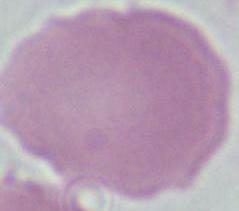
identification: erythrocyte
modality: micrograph
magnification: 1000x